Classify this cell by malaria status.
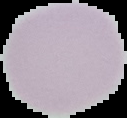
It is uninfected.

Summary:
  - Preparation: thin blood film
  - Image type: segmented cell region on a black background
  - Image size: 127×118 pixels